Identify the parasite.
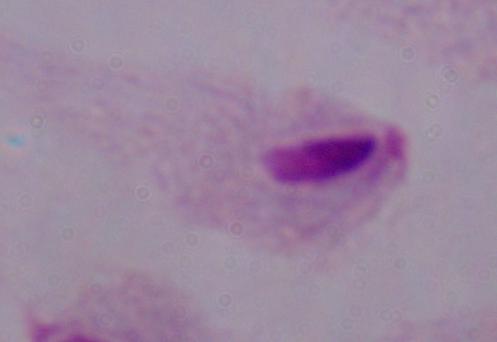

This is a trichomonad.

Summary:
  - Modality: micrograph
  - Magnification: 1000x